Mark where platelets are.
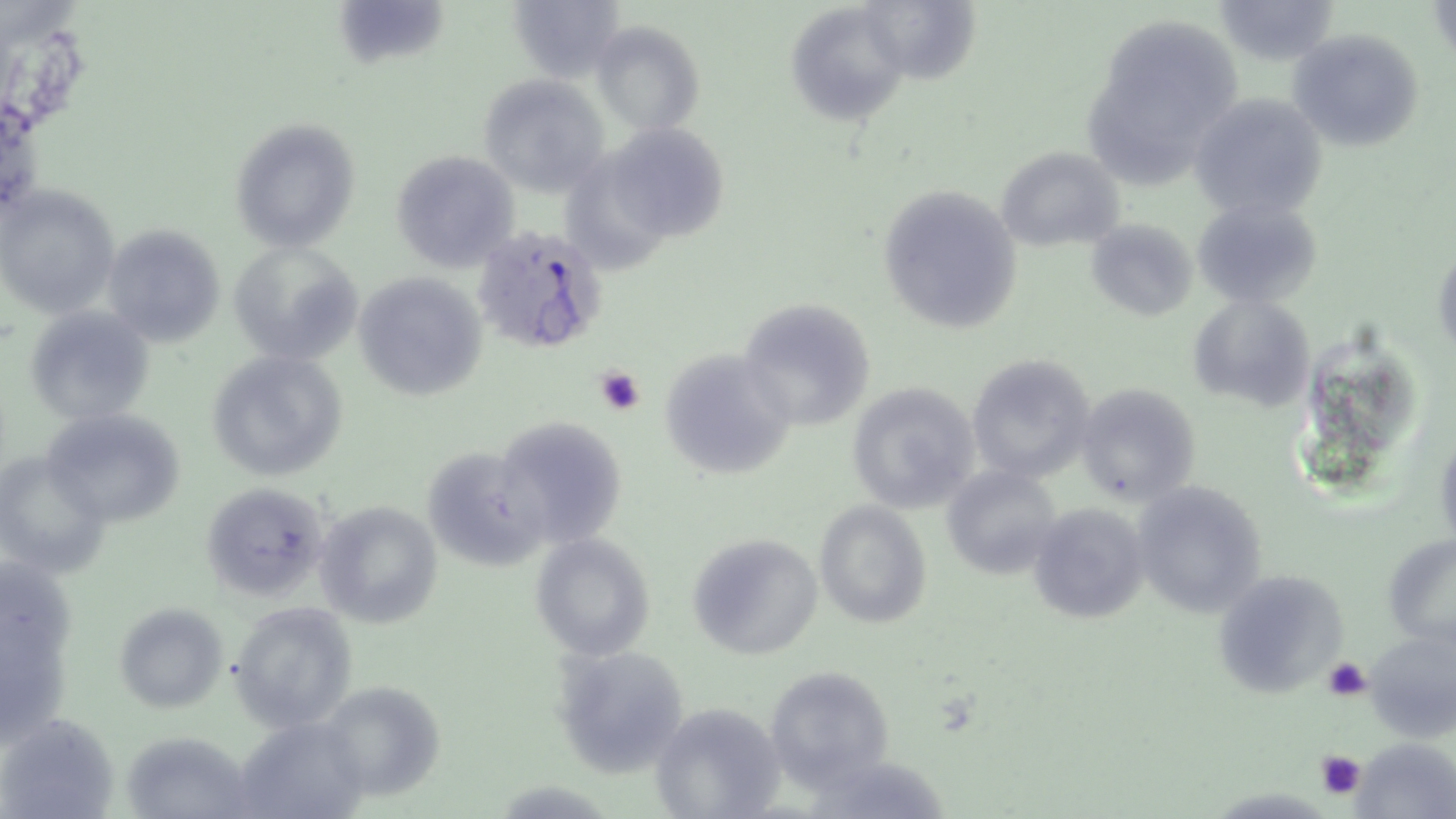

Approximate bounding boxes as (x1, y1, x2, y2) in pixels.
Platelets: (594, 364, 647, 416), (1322, 657, 1372, 702), (1314, 749, 1367, 804).

Summary:
  - Uninfected red blood cell locations: (330, 0, 469, 68), (1214, 0, 1338, 61), (505, 1, 625, 80), (866, 1, 987, 80), (1428, 1, 1453, 60), (788, 2, 908, 119), (592, 21, 704, 134), (1114, 24, 1249, 133), (1287, 28, 1424, 154), (477, 74, 610, 196), (1082, 78, 1195, 190), (1189, 92, 1327, 224), (230, 117, 363, 252), (622, 129, 737, 245), (995, 145, 1126, 252), (390, 151, 519, 273), (580, 162, 670, 283), (875, 182, 1024, 336), (0, 184, 121, 318), (1194, 197, 1322, 308), (1087, 219, 1194, 320), (101, 222, 227, 348), (229, 240, 366, 366), (1432, 246, 1455, 358), (353, 272, 487, 399), (1188, 295, 1315, 412), (736, 297, 879, 431), (25, 307, 156, 425), (659, 349, 796, 479), (206, 350, 349, 482), (965, 352, 1097, 486), (844, 380, 982, 514), (1074, 383, 1201, 506), (39, 405, 189, 529), (493, 415, 629, 549), (421, 443, 544, 572), (0, 448, 110, 576), (941, 466, 1063, 580), (1130, 480, 1269, 618), (200, 482, 332, 602), (313, 500, 443, 629), (814, 500, 931, 628), (1026, 502, 1149, 625), (686, 532, 822, 660), (530, 533, 656, 660), (1384, 533, 1454, 646), (1212, 569, 1350, 700), (231, 602, 360, 731), (114, 603, 226, 714), (1, 610, 66, 743), (1360, 625, 1455, 742), (553, 643, 693, 777), (762, 666, 894, 786), (318, 680, 448, 802), (648, 702, 783, 818), (1, 713, 118, 818), (236, 716, 370, 819), (1350, 737, 1456, 818), (812, 749, 963, 819)
  - Plasmodium falciparum-infected red blood cell locations: (473, 224, 612, 355)
  - Slide-level diagnosis: Plasmodium falciparum
  - Field of view: one of a larger specimen
  - Modality: light microscopy
  - Magnification: 1000x
  - Preparation: thin blood smear
  - Image size: 1456×819 pixels
  - Stain: May-Grünwald-Giemsa